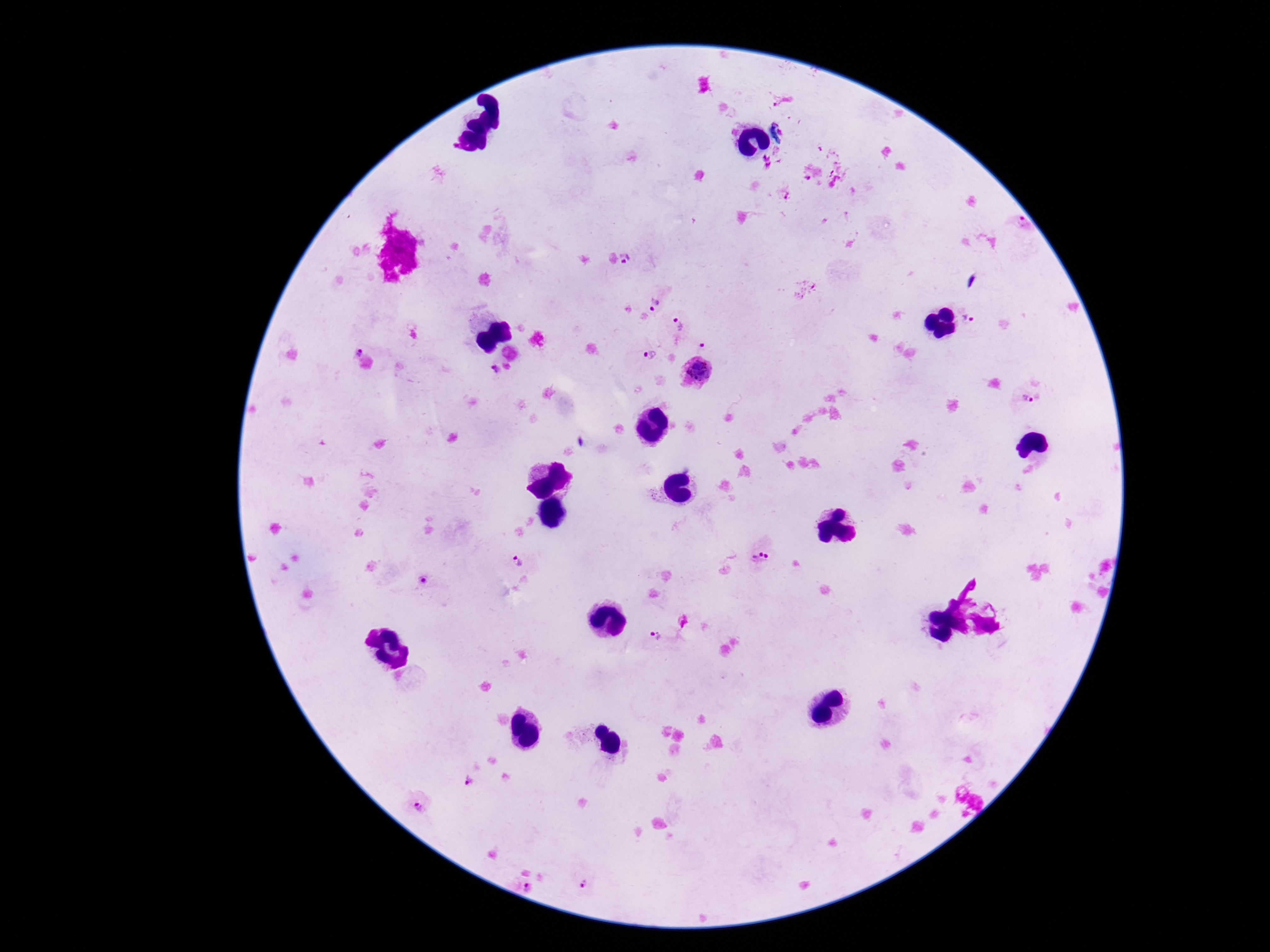
Approximate centers as [x, y] in pixels.
Summary:
  - Plasmodium parasite locations: [1019, 225], [632, 256], [655, 302], [968, 318], [680, 322], [707, 340], [357, 348], [647, 353], [699, 368], [494, 370], [1025, 397], [761, 554], [518, 562], [420, 582], [655, 635], [469, 780], [417, 805], [526, 885], [584, 885]
  - Preparation: thick peripheral-blood smear
  - Capture: smartphone camera through the microscope eyepiece
  - Patient malaria status: infected
  - Field of view: one from this slide
  - Stain: Giemsa
  - Image size: 1270×952 pixels
  - Magnification: 100x